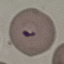
Result: malaria parasites detected. Giemsa stain. Thin blood film. Automatically extracted cell patch, resized to 64 × 64 pixels. Photographed with a smartphone camera at the microscope eyepiece.